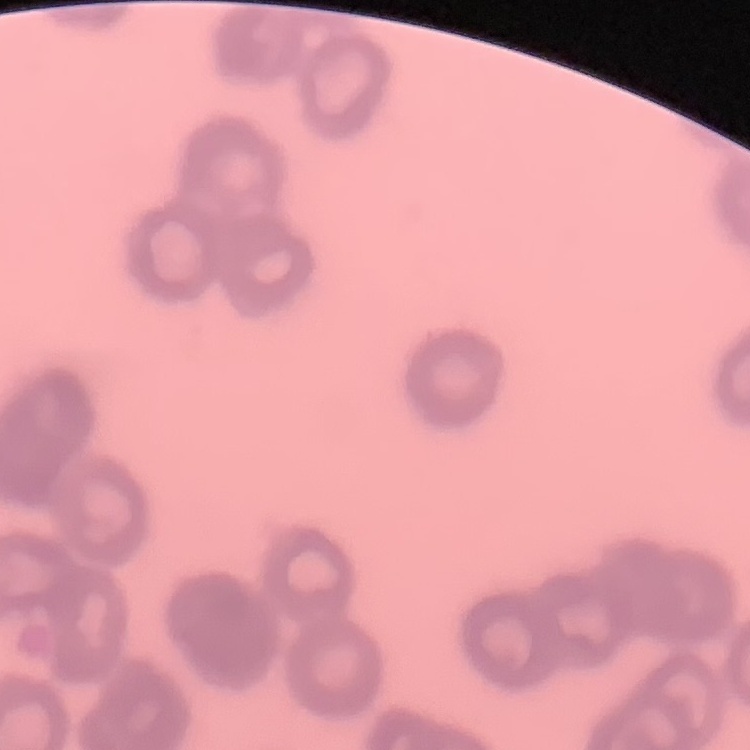
red blood cell morphology = rouleaux formation
stain = Field's or Giemsa
image type = square crop of a larger photomicrograph
preparation = thin blood film